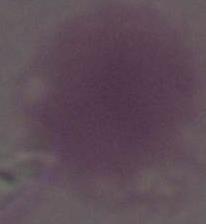
Summary:
  - Identification: red blood cell
  - Modality: micrograph
  - Magnification: 1000x